Give the preparation type.
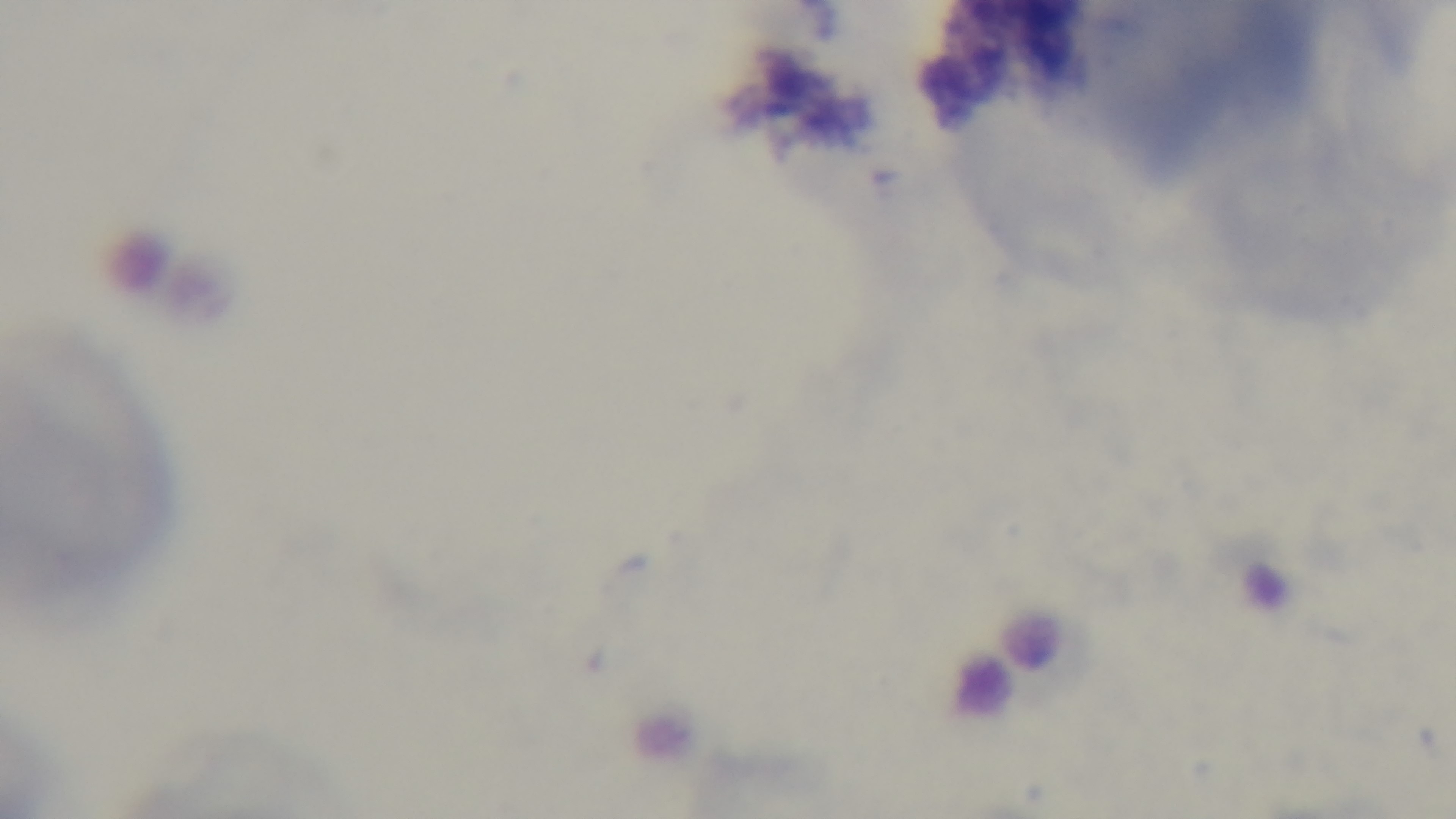
Thin.

{
  "capture": "mounted 4K digital camera",
  "objective": "100x oil immersion",
  "stain": "Giemsa",
  "field_of_view": "single",
  "modality": "light microscopy",
  "malaria_status": "negative"
}